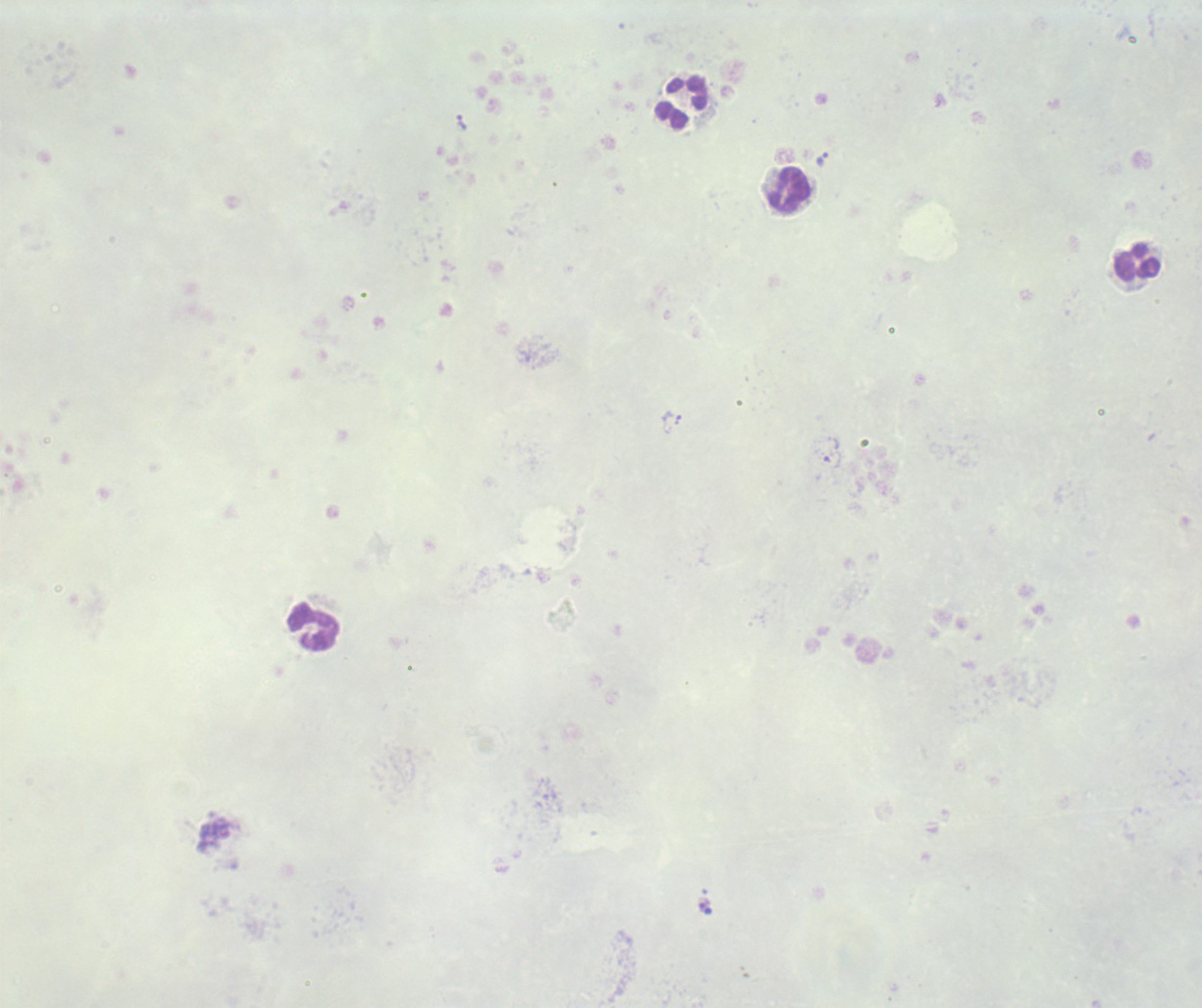 Approximate centers as (x, y) in pixels. Trophozoite locations: (462, 123), (823, 159), (673, 422), (832, 452). Leukocyte locations: (683, 101), (790, 192), (1137, 262), (312, 627). Image is 1202×1008 pixels. Background quality: poor. Result: malaria parasites identified. Captured at 100x magnification. Romanowsky stain. Thick blood smear. Previously used in a real diagnosis. One field from this slide. Coloration quality: bad.